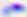
identification = Toxoplasma gondii
modality = micrograph
magnification = 400x